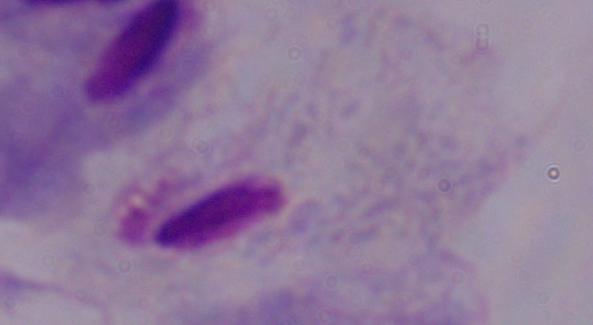 1000x magnification. Micrograph. A trichomonad is shown.